Give the position of every Plasmodium parasite.
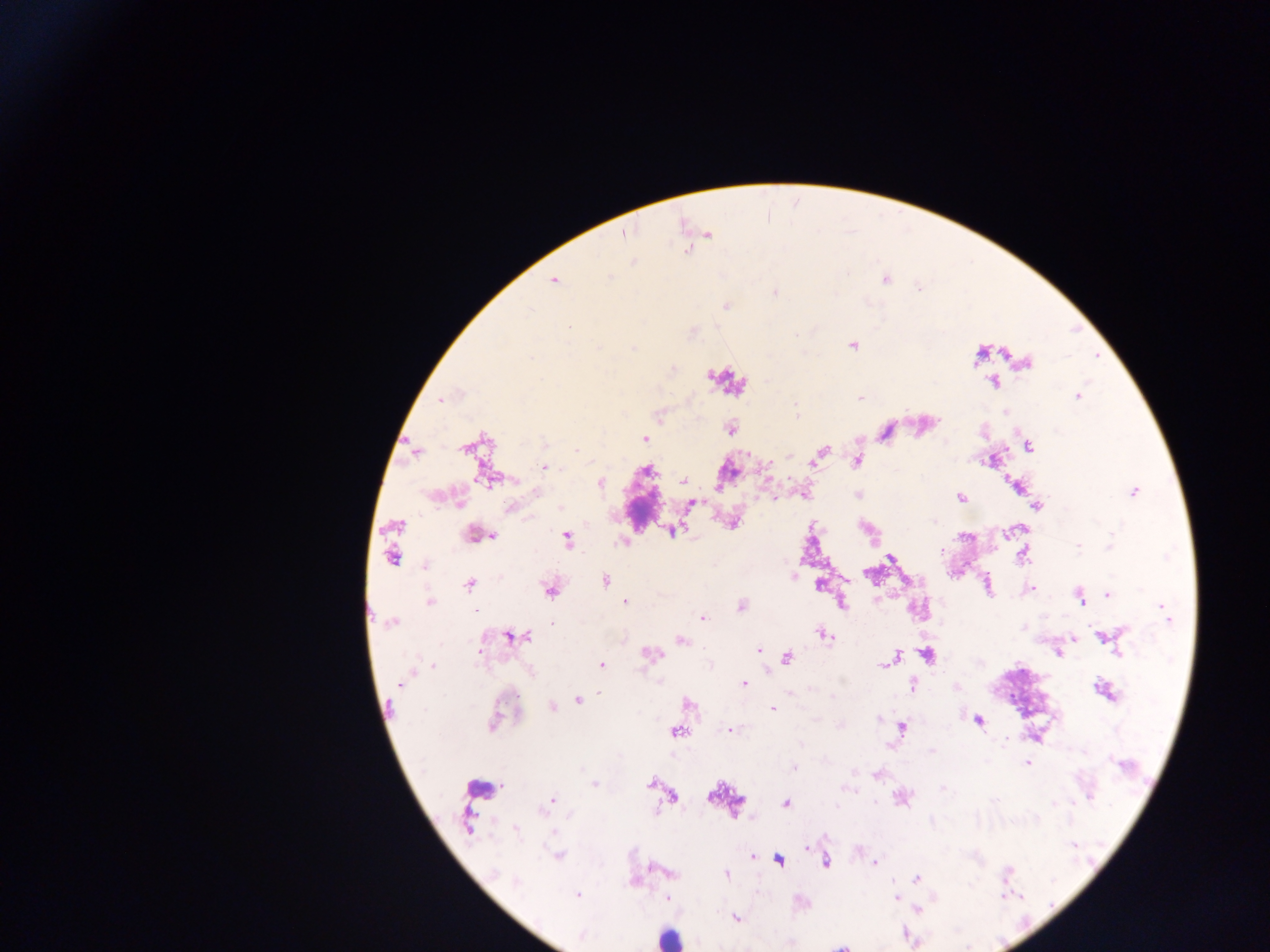
Approximate centers as {x, y} in pixels.
Plasmodium parasites: {623, 232}, {707, 234}, {688, 247}, {633, 262}, {554, 279}, {852, 345}, {979, 354}, {1026, 363}, {994, 381}, {1077, 395}, {860, 398}, {440, 399}, {796, 415}, {731, 429}, {885, 432}, {644, 438}, {471, 445}, {1028, 446}, {415, 449}, {821, 451}, {816, 458}, {857, 461}, {545, 466}, {490, 478}, {683, 481}, {598, 482}, {1017, 486}, {1133, 492}, {804, 494}, {858, 495}, {961, 497}, {690, 503}, {1036, 505}, {734, 521}, {672, 529}, {1008, 532}, {475, 534}, {566, 538}, {623, 542}, {941, 551}, {392, 553}, {1022, 554}, {890, 557}, {425, 565}, {604, 581}, {819, 583}, {468, 584}, {549, 588}, {1029, 589}, {1108, 594}, {1079, 596}, {430, 601}, {625, 601}, {840, 602}, {740, 606}, {1165, 610}, {702, 618}, {392, 622}, {823, 634}, {514, 636}, {1103, 636}, {1073, 638}, {680, 640}, {757, 651}, {1058, 652}, {650, 654}, {926, 654}, {786, 657}, {891, 658}, {885, 662}, {601, 664}, {432, 665}, {743, 684}, {913, 685}, {1104, 690}, {599, 693}, {579, 699}, {558, 704}, {687, 704}, {551, 706}, {772, 709}, {977, 719}, {900, 727}, {728, 729}, {676, 732}, {1027, 763}, {876, 774}, {651, 783}, {594, 784}, {671, 796}, {552, 800}, {785, 803}, {468, 820}, {558, 855}, {751, 856}, {778, 860}, {825, 861}, {874, 862}, {668, 873}, {726, 874}, {916, 878}, {633, 881}, {577, 895}, {668, 898}, {896, 898}, {734, 917}, {841, 946}.

Summary:
  - Leukocyte locations: {479, 785}, {666, 938}
  - Image size: 1270×952 pixels
  - Preparation: thick blood smear
  - Field of view: single
  - Capture: mobile-phone photograph through a microscope
  - Country: Ghana